Locate every malaria parasite and every leukocyte.
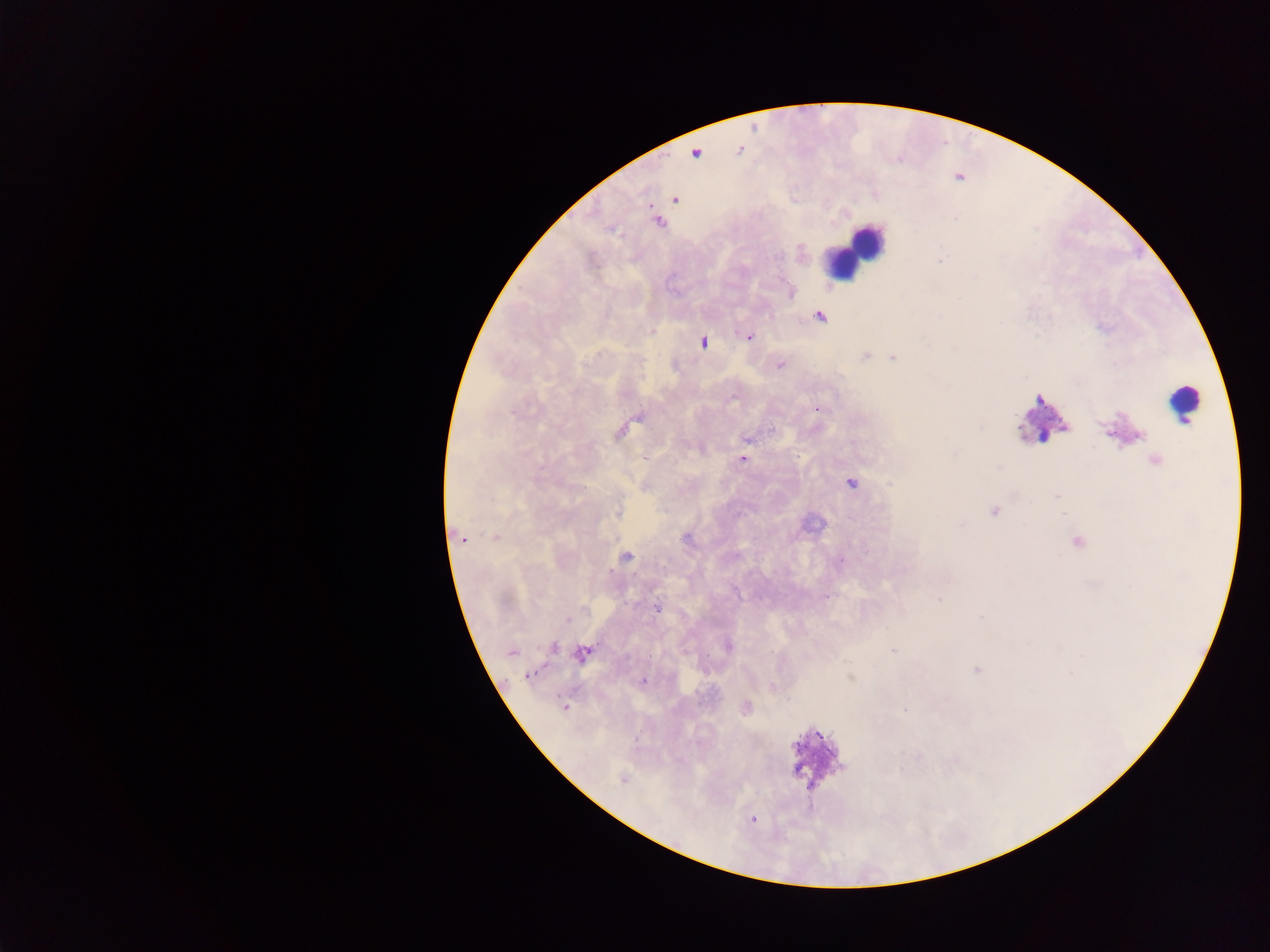

Approximate centers as {x, y} in pixels.
Malaria parasites: {739, 150}, {695, 153}, {960, 175}, {674, 200}, {657, 221}, {788, 292}, {819, 316}, {748, 336}, {702, 342}, {866, 355}, {893, 357}, {779, 365}, {816, 408}, {622, 429}, {747, 438}, {742, 459}, {851, 482}, {618, 512}, {457, 536}, {495, 537}, {625, 557}, {827, 595}, {656, 607}, {552, 646}, {894, 650}, {511, 652}, {582, 653}, {978, 669}, {527, 674}, {643, 680}, {565, 707}, {905, 709}, {750, 819}.
Leukocytes: {870, 238}, {834, 263}, {1184, 404}, {1041, 419}, {815, 759}.

{
  "country": "Ghana",
  "preparation": "thick blood film",
  "capture": "mobile-phone photograph through a microscope",
  "field_of_view": "single",
  "image_size": "1270×952 pixels"
}